Assess the morphology of the red blood cells.
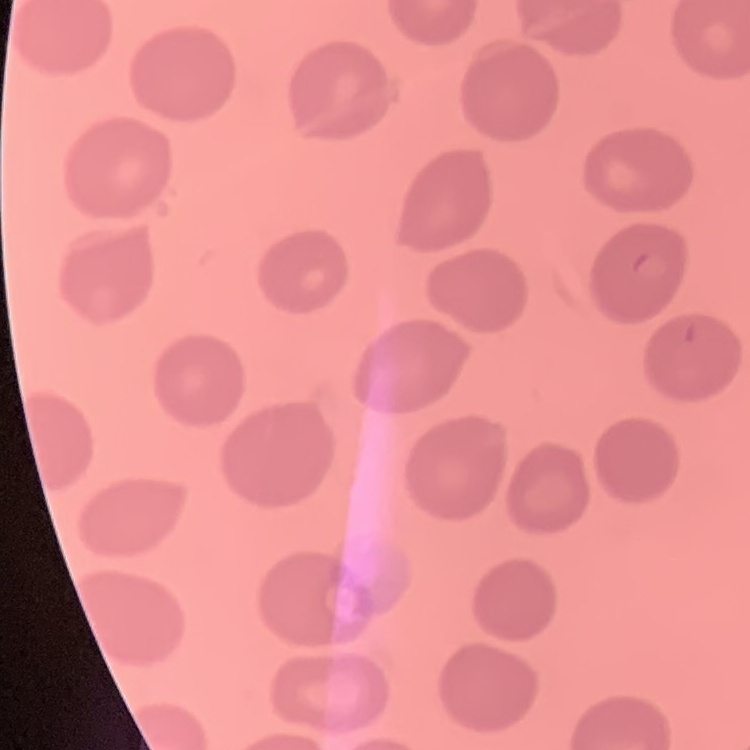

No rouleaux formation.

Summary:
  - Image type: square crop of a larger photomicrograph
  - Stain: Field's or Giemsa
  - Preparation: thin peripheral smear